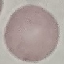
Summary:
  - Result: no malaria parasites seen
  - Preparation: thin smear
  - Image type: automatically extracted cell patch, resized to 64 × 64 pixels
  - Stain: Giemsa
  - Capture: smartphone camera at the microscope eyepiece